Locate every malaria parasite.
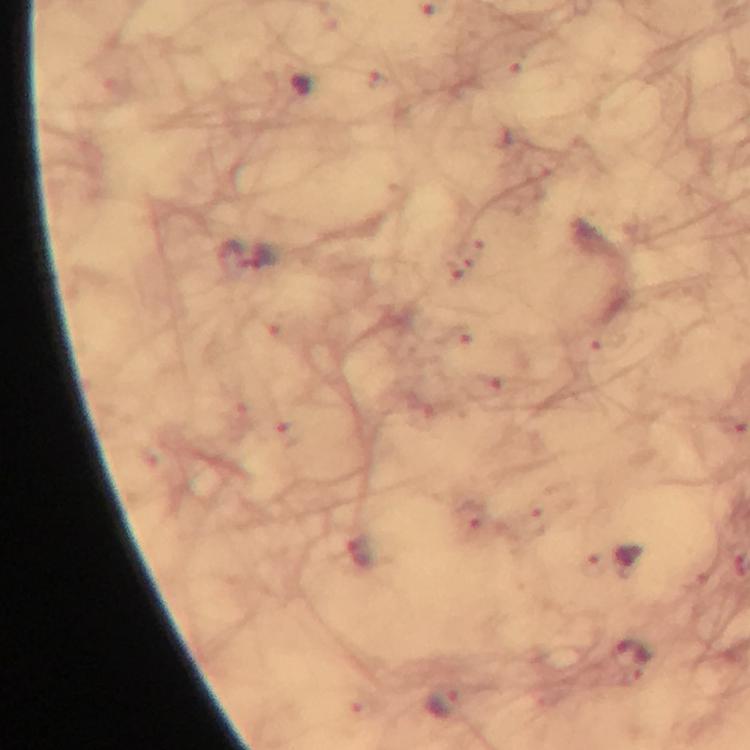
Approximate centers as (x, y) in pixels.
Malaria parasites: (229, 256), (263, 257), (359, 551), (630, 659), (443, 704).

From a malaria diagnostic workup. Thick blood smear. 100x magnification. Immersion oil was used. A crop from one field of view. Giemsa-stained preparation. Photographed through the microscope with a smartphone camera. Image is 750×750 pixels.